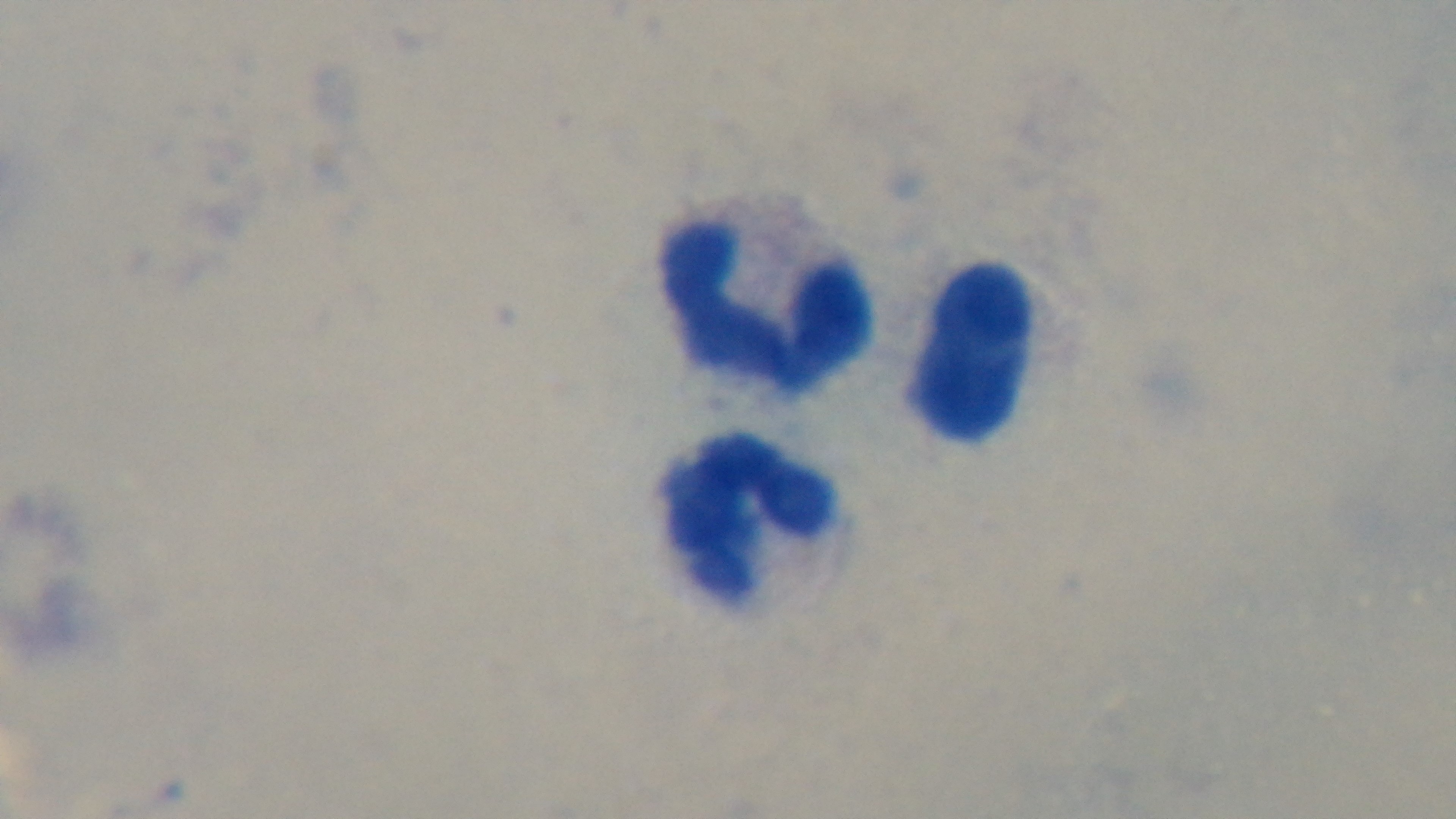
Summary:
  - Stain: Giemsa
  - Capture: mounted 4K digital camera
  - Preparation: thick
  - Field of view: one from the slide
  - Objective: 100x oil immersion
  - Malaria status: uninfected
  - Modality: light microscopy